Report the malaria status of this cell.
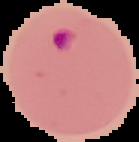

Parasitized.

From a thin blood film. Image is 139×142 pixels. Segmented cell region on a black background.